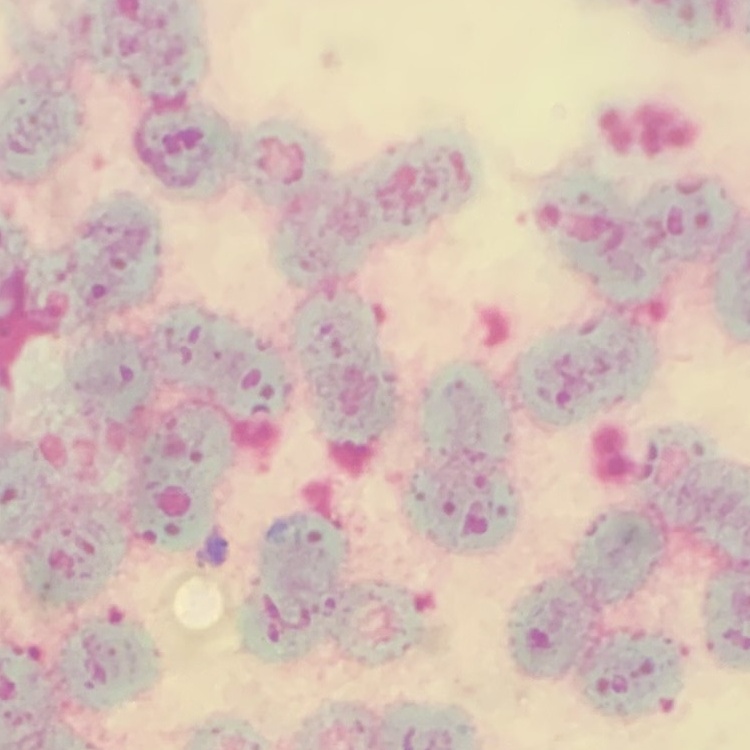

The red blood cells exhibit rouleaux formation. One tile cut from a larger photomicrograph. Field's or Giemsa stain. Thin blood smear.